Locate platelets.
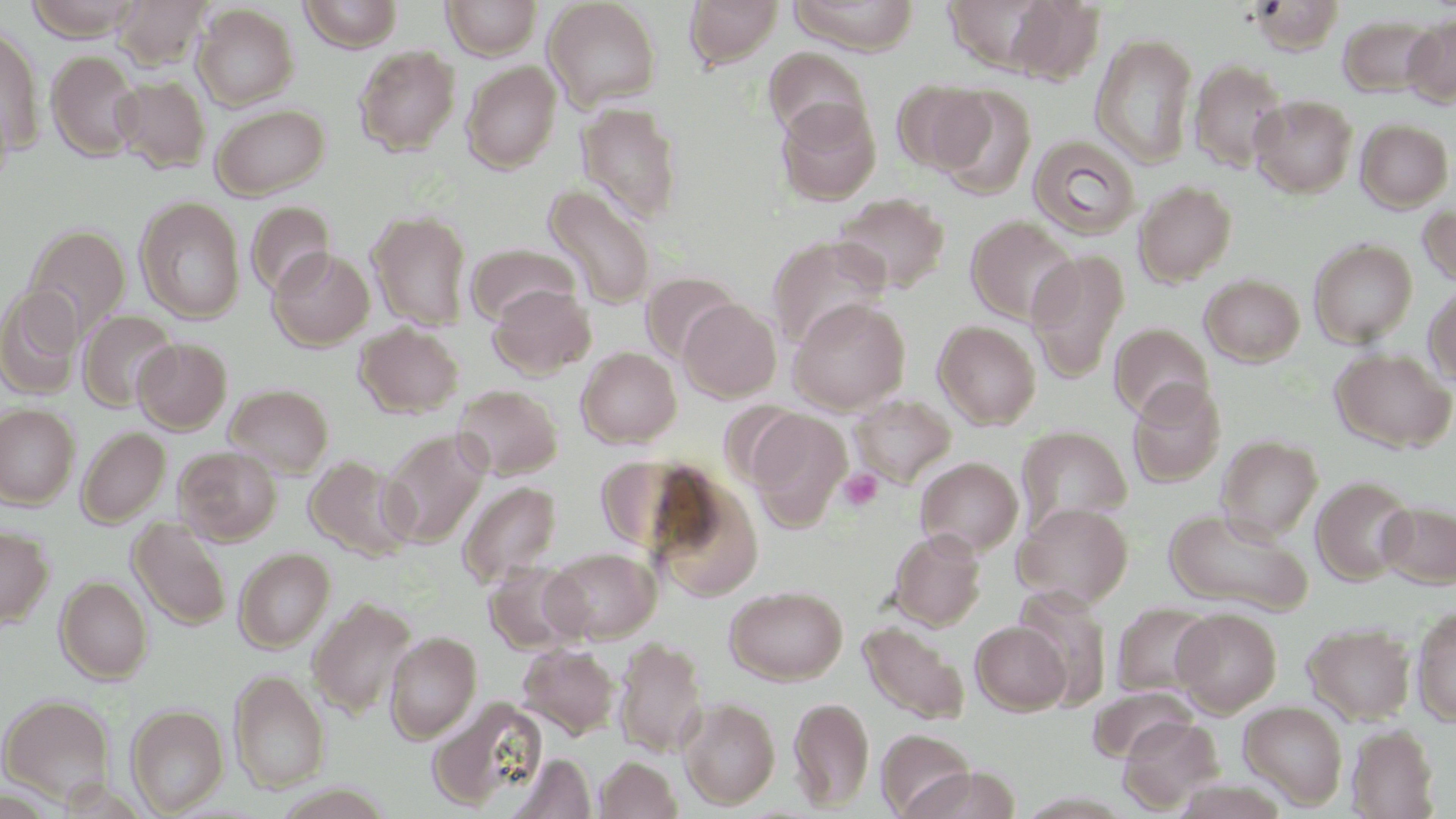

Approximate bounding boxes as (x1,y1)-(x2,y2) corner pairs in pixels.
Platelets: (837,468)-(882,511).

Uninfected red blood cell locations: (23,0)-(142,41), (113,0)-(210,69), (298,0)-(404,52), (442,0)-(542,59), (543,0)-(661,111), (684,0)-(784,70), (785,0)-(920,54), (940,0)-(1068,75), (1005,2)-(1105,84), (193,4)-(299,109), (1338,15)-(1438,97), (1401,15)-(1456,107), (1,23)-(45,155), (1091,33)-(1198,169), (353,45)-(460,156), (763,46)-(872,147), (46,51)-(143,161), (1188,57)-(1289,173), (461,60)-(562,174), (113,75)-(211,173), (891,80)-(993,175), (933,86)-(1036,198), (1250,94)-(1358,197), (775,99)-(881,206), (575,101)-(683,225), (211,103)-(329,199), (1356,119)-(1454,211), (1028,135)-(1141,239), (1134,180)-(1238,286), (544,184)-(656,309), (833,192)-(951,296), (134,196)-(245,323), (246,201)-(335,298), (1418,202)-(1456,290), (368,210)-(473,331), (966,215)-(1079,326), (24,224)-(131,334), (767,234)-(891,348), (1309,238)-(1418,347), (466,243)-(580,326), (268,248)-(374,350), (1026,249)-(1130,383), (641,270)-(739,363), (1200,274)-(1305,367), (1423,283)-(1456,388), (488,284)-(596,379), (0,286)-(85,399), (789,297)-(910,414), (679,298)-(781,402), (78,309)-(179,411), (934,320)-(1041,429), (355,322)-(464,418), (1110,322)-(1213,422), (134,338)-(232,434), (577,347)-(681,447), (1331,348)-(1456,452), (1126,380)-(1225,488), (224,383)-(334,478), (453,384)-(563,479), (850,393)-(956,488), (0,403)-(79,509), (748,410)-(851,530), (1016,425)-(1132,531), (76,427)-(170,527), (380,428)-(490,548), (1216,435)-(1323,542), (174,445)-(283,545), (304,455)-(414,560), (916,456)-(1023,556), (1311,475)-(1416,585), (650,476)-(765,601), (458,481)-(561,585), (1378,500)-(1456,588), (1013,501)-(1133,607), (1163,507)-(1312,615), (128,516)-(231,631), (0,525)-(54,630), (888,529)-(986,630), (234,547)-(334,652), (545,547)-(661,643), (484,562)-(587,655), (55,576)-(152,684), (725,585)-(848,684), (1012,587)-(1115,710), (308,596)-(417,720), (1112,602)-(1217,699), (1411,605)-(1456,726), (1172,608)-(1282,715), (972,621)-(1071,715), (1302,622)-(1416,725), (859,623)-(968,725), (385,631)-(482,743), (615,636)-(707,758), (517,643)-(619,738), (229,669)-(330,793), (1088,687)-(1195,764), (0,693)-(116,805), (789,696)-(874,810), (429,698)-(547,811), (679,698)-(780,809), (1239,701)-(1348,809), (125,704)-(229,815), (1117,715)-(1222,812), (1346,724)-(1441,818), (877,729)-(976,817), (508,752)-(596,818), (594,756)-(682,819), (1174,777)-(1290,818). Slide-level diagnosis: no evidence of blood parasites. Optical microscopy. Thin blood smear. May-Grünwald-Giemsa-stained preparation. One field of a larger specimen. Image is 1456×819 pixels. Captured at 1000x magnification.